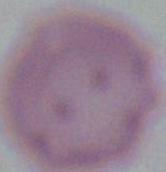
Micrograph. A red blood cell is seen. 1000x magnification.